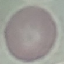
{
  "malaria_status": "uninfected",
  "capture": "smartphone through the microscope eyepiece",
  "image_type": "cell patch, automatically extracted from a larger field of view and resized to 64 × 64 pixels",
  "preparation": "thin blood smear",
  "stain": "Giemsa"
}